Describe the morphology of the erythrocytes.
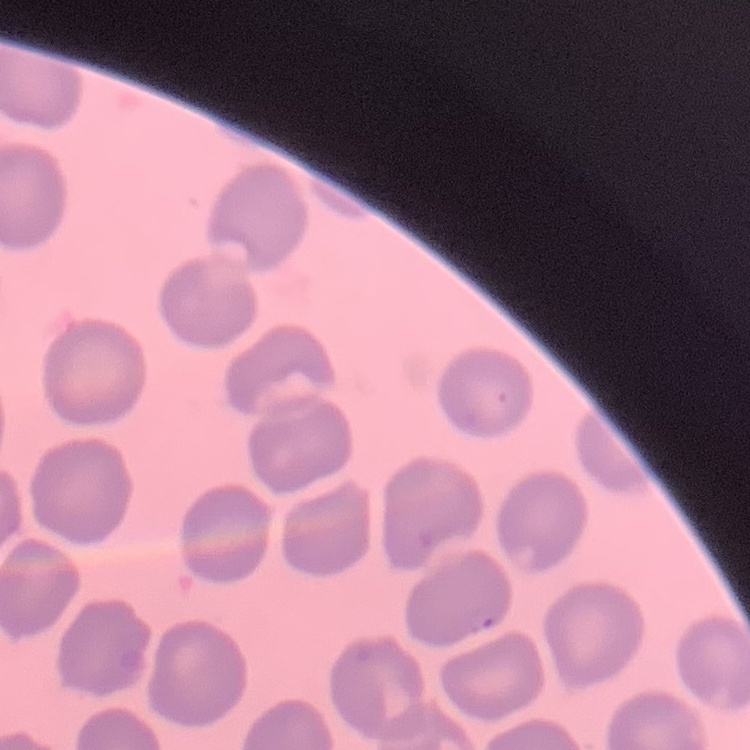
They show no rouleaux formation.

stain = Field's or Giemsa
preparation = thin blood film
image type = one tile cut from a larger photomicrograph